Assess this cell for malaria.
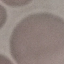

Uninfected.

Summary:
  - Image type: cell patch, automatically extracted from a larger field of view and resized to 64 × 64 pixels
  - Stain: Giemsa
  - Preparation: thin smear
  - Capture: smartphone through the microscope eyepiece